Assess this cell for malaria.
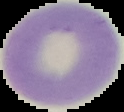
It is uninfected.

{
  "image_size": "124×112 pixels",
  "preparation": "thin blood smear",
  "image_type": "segmented cell region with the area outside set to black"
}